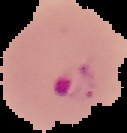

Summary:
  - Image type: segmented cell region on a black background
  - Preparation: thin blood smear
  - Image size: 127×133 pixels
  - Malaria status: parasitized